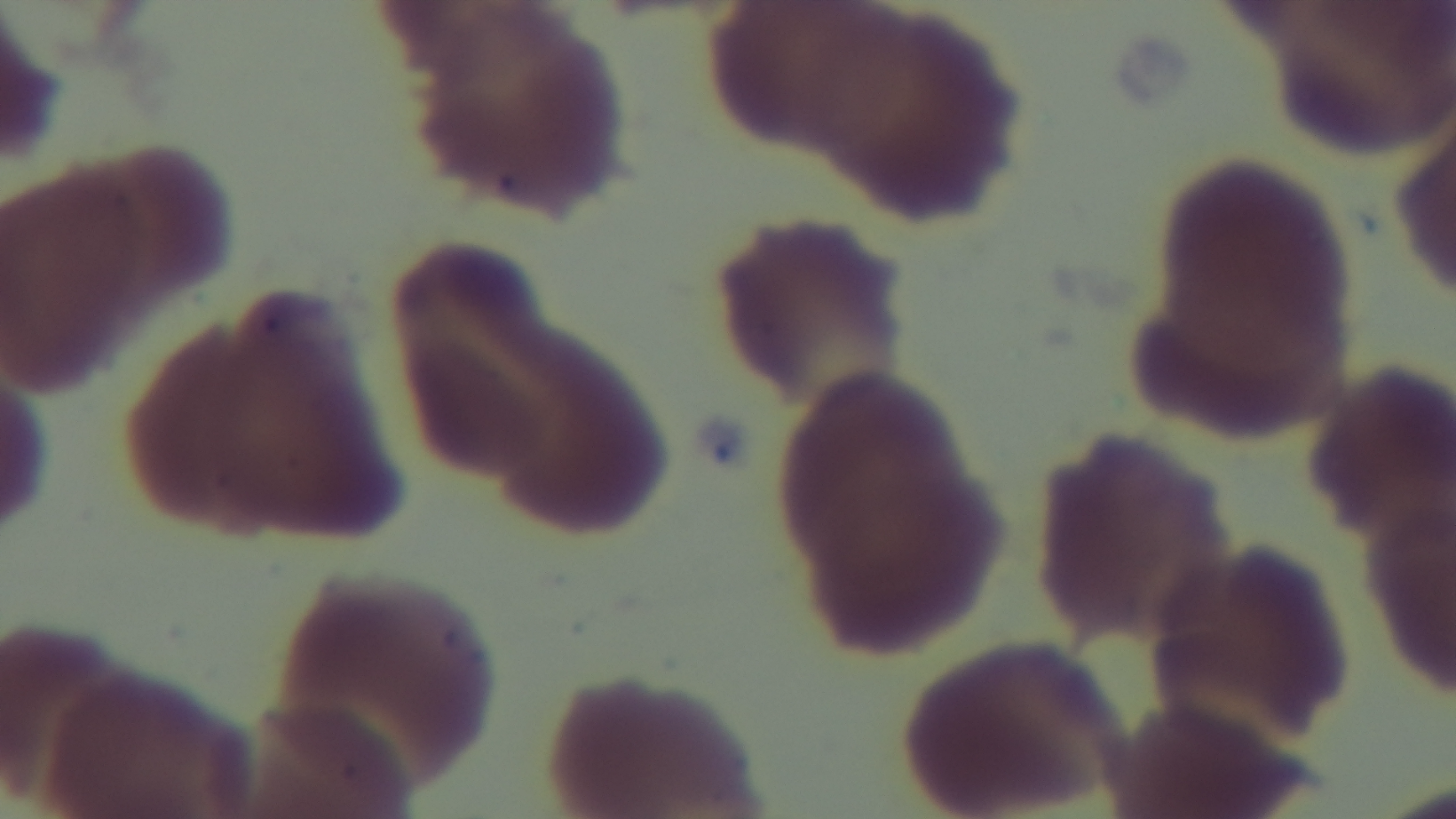
preparation = thin
capture = mounted 4K digital camera
objective = 100x oil immersion
malaria status = negative
field of view = single
stain = Giemsa
modality = light microscopy